Comment on the morphology of the erythrocytes.
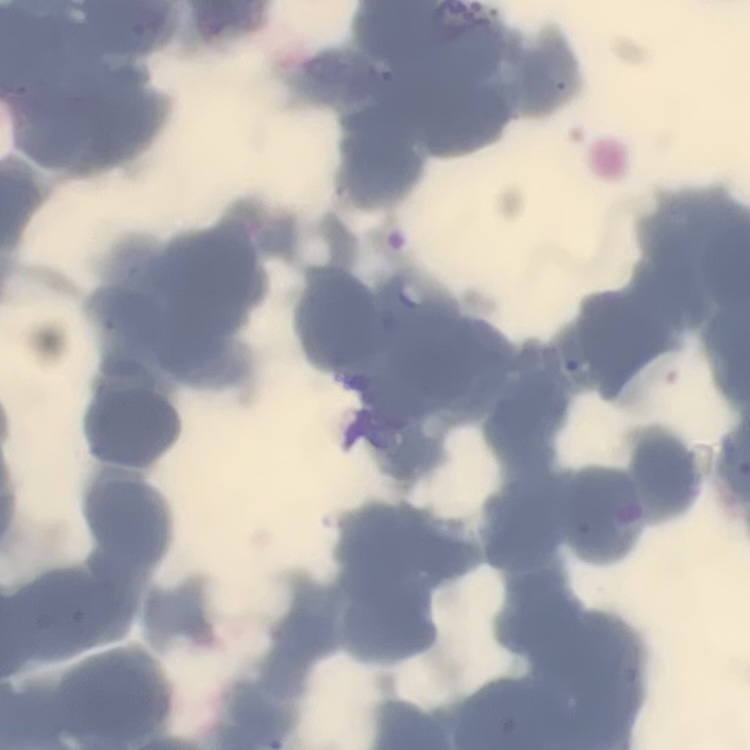

Rouleaux formation.

One tile cut from a larger photomicrograph. Field's or Giemsa stain. Thin blood film.